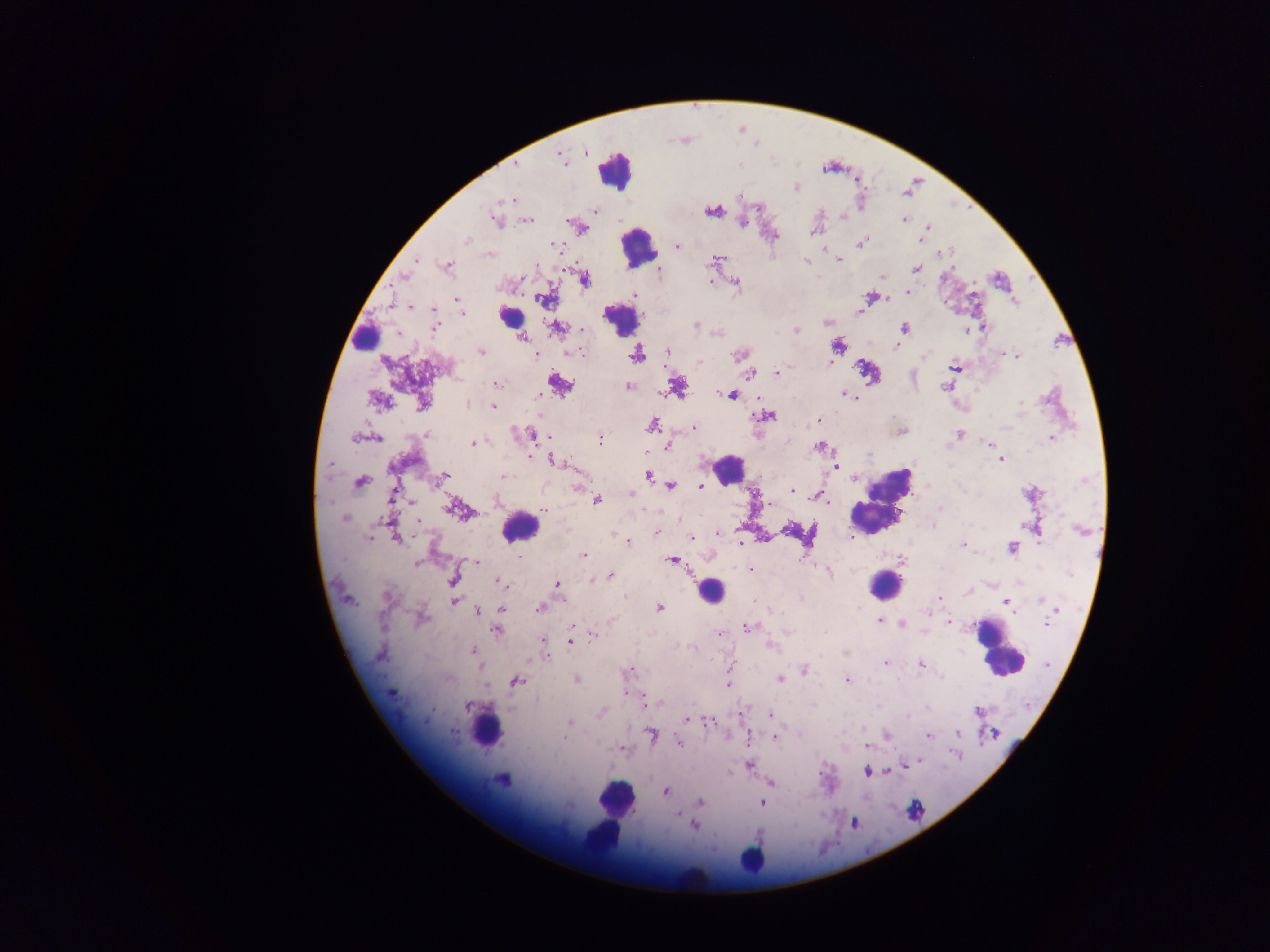

country = Ghana
malaria parasite locations = approximate centers as (x, y) in pixels: (585, 152), (561, 158), (515, 164), (796, 188), (511, 199), (594, 211), (712, 212), (842, 216), (904, 219), (528, 220), (495, 222), (742, 222), (927, 227), (583, 229), (814, 231), (775, 236), (467, 240), (920, 240), (863, 241), (553, 245), (677, 246), (941, 253), (490, 254), (416, 260), (839, 260), (714, 261), (806, 261), (448, 266), (917, 269), (403, 276), (882, 277), (521, 279), (585, 280), (710, 281), (736, 283), (908, 292), (635, 295), (870, 297), (457, 299), (546, 299), (411, 307), (860, 311), (463, 313), (827, 322), (435, 325), (695, 325), (983, 327), (556, 328), (904, 329), (582, 331), (796, 331), (967, 331), (523, 337), (838, 346), (897, 347), (667, 351), (481, 352), (580, 353), (535, 355), (637, 355), (738, 355), (1008, 355), (1017, 356), (923, 357), (955, 367), (777, 372), (750, 373), (496, 383), (560, 385), (628, 386), (945, 387), (678, 388), (846, 394), (732, 395), (538, 397), (379, 401), (1021, 403), (422, 404), (467, 405), (493, 406), (768, 416), (819, 420), (653, 425), (694, 428), (530, 433), (427, 434), (959, 434), (354, 437), (377, 438), (600, 438), (1051, 438), (472, 443), (987, 444), (668, 446), (820, 447), (531, 457), (1001, 460), (557, 462), (330, 464), (836, 466), (443, 476), (503, 476), (647, 476), (360, 481), (1084, 481), (671, 484), (701, 485), (577, 487), (791, 490), (631, 494), (758, 494), (817, 495), (597, 500), (769, 503), (939, 508), (455, 509), (545, 510), (344, 518), (934, 526), (1080, 530), (656, 532), (718, 534), (852, 536), (369, 538), (397, 538), (693, 538), (627, 541), (740, 543), (963, 545), (1012, 548), (584, 555), (517, 556), (672, 560), (417, 563), (476, 563), (750, 570), (829, 573), (610, 576), (453, 579), (592, 579), (501, 583), (557, 585), (968, 592), (624, 595), (387, 596), (940, 597), (1041, 600), (455, 601), (1007, 602), (1045, 603), (659, 608), (539, 609), (502, 610), (477, 611), (1054, 612), (422, 618), (880, 621), (950, 622), (1047, 623), (903, 624), (748, 627), (497, 630), (721, 633), (594, 635), (571, 641), (543, 643), (772, 645), (545, 650), (474, 651), (381, 655), (885, 664), (920, 665), (804, 669), (628, 672), (780, 679), (576, 680), (516, 681), (847, 681), (728, 683), (391, 694), (628, 694), (651, 703), (467, 707), (978, 712), (601, 714), (770, 715), (687, 720), (570, 722), (709, 723), (958, 733), (652, 735), (887, 736), (928, 736), (774, 738), (679, 743), (868, 745), (622, 749), (750, 764), (867, 772), (501, 780), (666, 791), (700, 802), (762, 803), (678, 814), (694, 826)
image size = 1270×952 pixels
field of view = single
leukocyte locations = approximate centers as (x, y) in pixels: (615, 168), (638, 248), (508, 311), (618, 320), (365, 336), (730, 469), (883, 501), (519, 528), (885, 585), (710, 591), (997, 648), (487, 724), (615, 798), (601, 836), (758, 856), (690, 881)
capture = mobile-phone photograph through a microscope
preparation = thick blood film